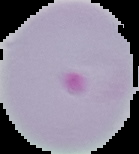
From a thin blood film. The area outside the segmented cell region is set to black. Result: malaria parasites detected. Image is 139×154 pixels.